Give the extent of all Trypanosoma brucei.
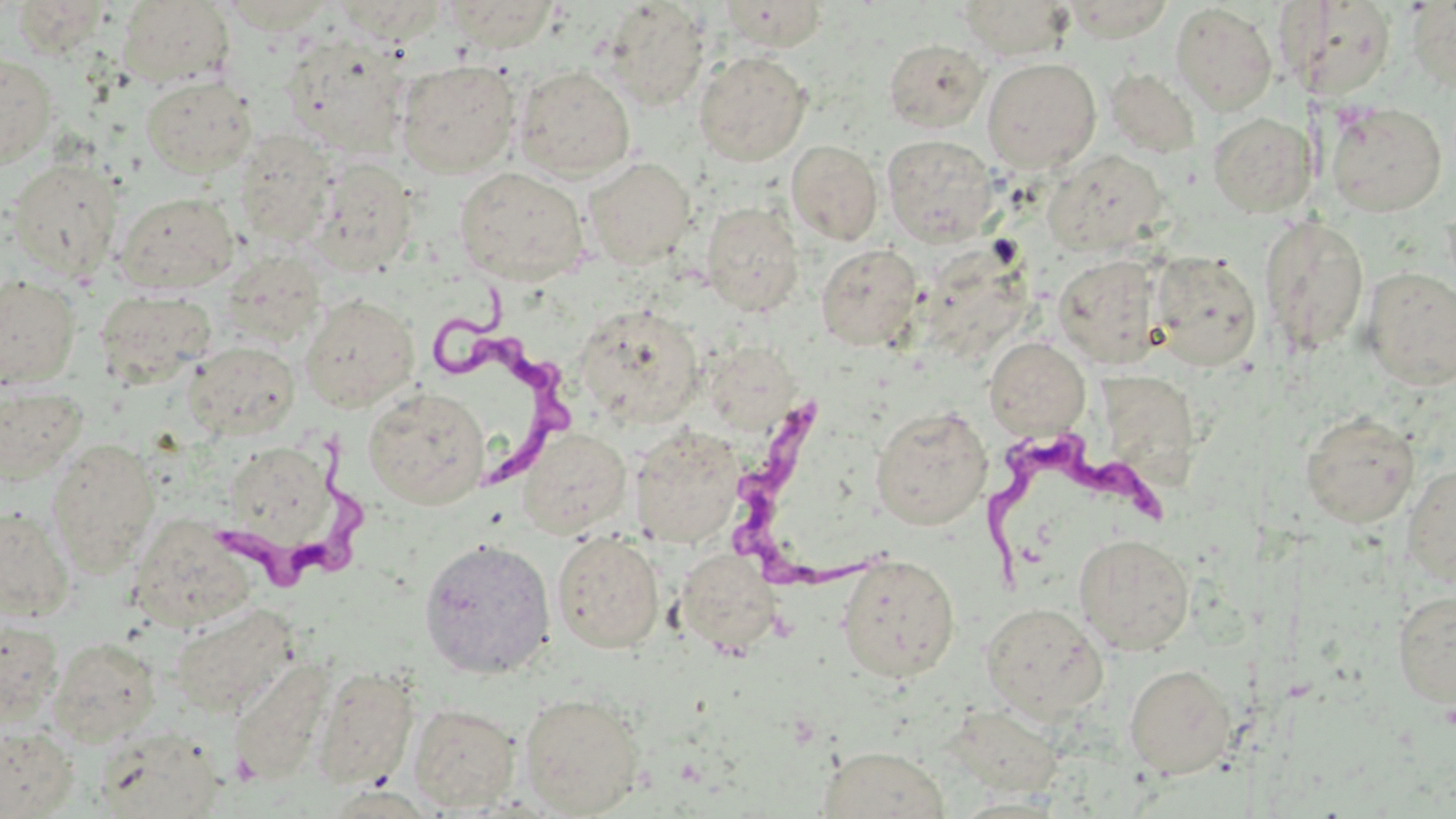

Approximate bounding boxes as named x1/y1/x2/y2 corners in pixels.
Trypanosoma brucei: (x1=428, y1=283, x2=575, y2=495), (x1=732, y1=404, x2=874, y2=600), (x1=208, y1=424, x2=374, y2=605), (x1=971, y1=427, x2=1173, y2=589).

slide-level diagnosis = Trypanosoma brucei
field of view = one of a larger specimen
modality = optical microscopy
preparation = thin blood smear
uninfected red blood cell locations = approximate bounding boxes as named x1/y1/x2/y2 corners in pixels: (x1=956, y1=0, x2=1076, y2=60), (x1=1064, y1=0, x2=1174, y2=42), (x1=1406, y1=0, x2=1456, y2=95), (x1=10, y1=1, x2=111, y2=57), (x1=116, y1=1, x2=235, y2=89), (x1=218, y1=1, x2=338, y2=35), (x1=332, y1=1, x2=449, y2=44), (x1=444, y1=1, x2=559, y2=52), (x1=599, y1=1, x2=711, y2=111), (x1=715, y1=1, x2=829, y2=51), (x1=1284, y1=2, x2=1398, y2=100), (x1=1170, y1=3, x2=1278, y2=115), (x1=279, y1=33, x2=411, y2=156), (x1=883, y1=39, x2=990, y2=133), (x1=694, y1=51, x2=812, y2=166), (x1=0, y1=52, x2=58, y2=168), (x1=982, y1=57, x2=1102, y2=174), (x1=396, y1=59, x2=521, y2=178), (x1=514, y1=65, x2=636, y2=180), (x1=1105, y1=67, x2=1200, y2=157), (x1=140, y1=75, x2=257, y2=177), (x1=1326, y1=101, x2=1447, y2=216), (x1=1207, y1=113, x2=1317, y2=217), (x1=233, y1=130, x2=338, y2=248), (x1=881, y1=134, x2=998, y2=246), (x1=786, y1=140, x2=883, y2=245), (x1=1045, y1=149, x2=1168, y2=254), (x1=4, y1=157, x2=124, y2=281), (x1=583, y1=157, x2=697, y2=269), (x1=308, y1=158, x2=418, y2=276), (x1=454, y1=167, x2=589, y2=286), (x1=115, y1=191, x2=239, y2=295), (x1=701, y1=202, x2=805, y2=316), (x1=1259, y1=214, x2=1369, y2=356), (x1=816, y1=244, x2=923, y2=351), (x1=219, y1=250, x2=328, y2=348), (x1=1149, y1=252, x2=1262, y2=371), (x1=1053, y1=254, x2=1166, y2=368), (x1=1361, y1=267, x2=1456, y2=389), (x1=0, y1=273, x2=81, y2=390), (x1=93, y1=289, x2=216, y2=385), (x1=300, y1=293, x2=420, y2=411), (x1=574, y1=303, x2=705, y2=429), (x1=984, y1=336, x2=1091, y2=439), (x1=186, y1=342, x2=300, y2=439), (x1=704, y1=342, x2=800, y2=432), (x1=1094, y1=371, x2=1197, y2=495), (x1=0, y1=384, x2=88, y2=484), (x1=363, y1=387, x2=490, y2=508), (x1=870, y1=405, x2=993, y2=530), (x1=1299, y1=410, x2=1420, y2=528), (x1=628, y1=425, x2=746, y2=548), (x1=516, y1=426, x2=631, y2=539), (x1=46, y1=438, x2=161, y2=572), (x1=228, y1=450, x2=334, y2=545), (x1=1402, y1=463, x2=1455, y2=587), (x1=0, y1=505, x2=75, y2=622), (x1=129, y1=515, x2=259, y2=633), (x1=552, y1=530, x2=665, y2=653), (x1=1073, y1=533, x2=1195, y2=655), (x1=418, y1=537, x2=556, y2=679), (x1=673, y1=549, x2=784, y2=656), (x1=836, y1=554, x2=960, y2=683), (x1=1393, y1=589, x2=1456, y2=708), (x1=169, y1=603, x2=302, y2=718), (x1=980, y1=603, x2=1108, y2=721), (x1=0, y1=616, x2=63, y2=724), (x1=47, y1=637, x2=161, y2=746), (x1=227, y1=658, x2=334, y2=787), (x1=1124, y1=663, x2=1236, y2=778), (x1=311, y1=665, x2=420, y2=790), (x1=520, y1=692, x2=646, y2=817), (x1=408, y1=703, x2=522, y2=813), (x1=0, y1=725, x2=77, y2=817), (x1=93, y1=725, x2=227, y2=819), (x1=817, y1=746, x2=951, y2=819)
image size = 1456×819 pixels
stain = May-Grünwald-Giemsa
magnification = 1000x